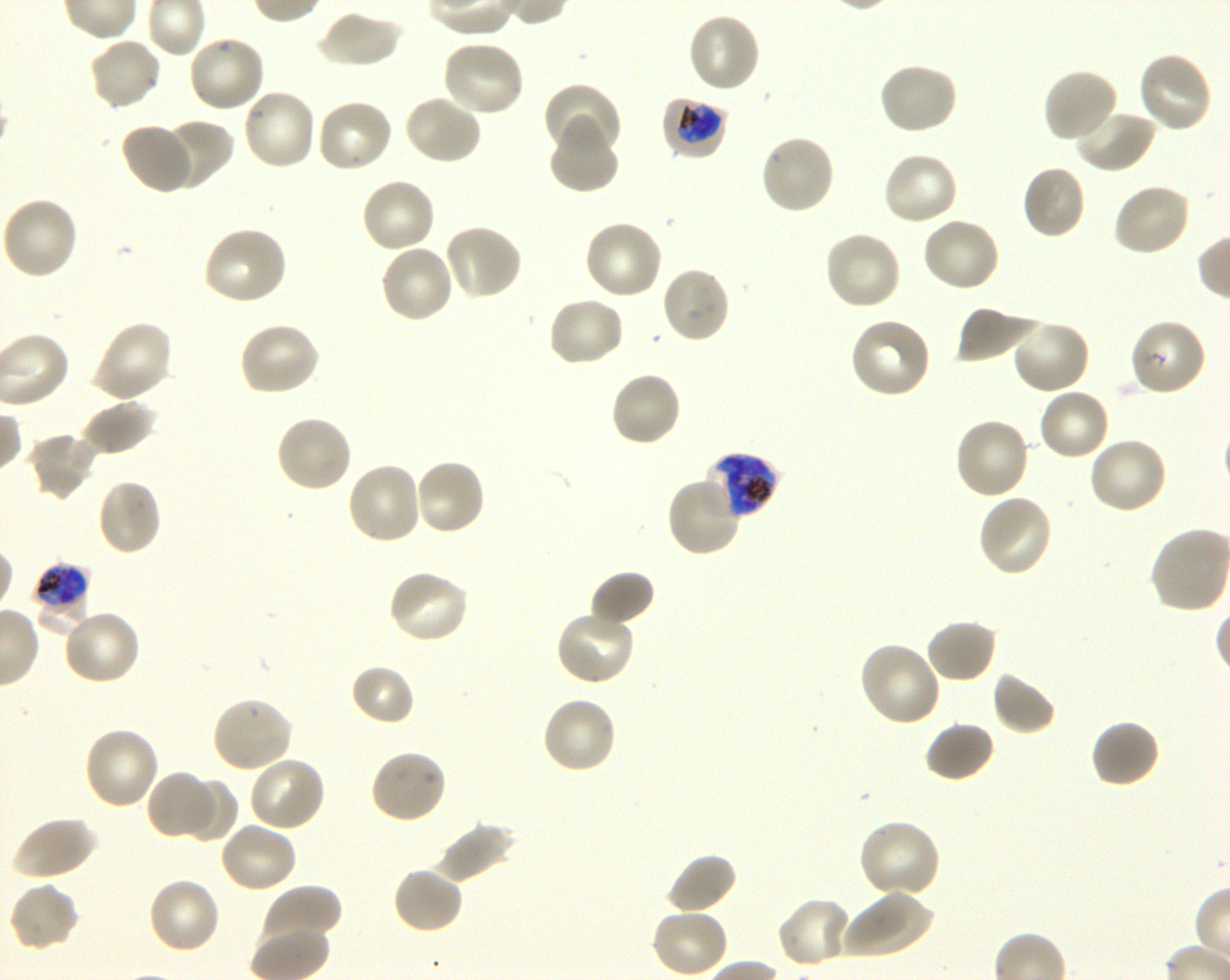

Approximate bounding rectangles given as corner coordinates in pixels from the top-left. Not every red blood cell is marked. A life-cycle stage — or a range of stages, where the recorded stages span more than one — follows each staged infected red blood cell.
Summary:
  - Locations of infected red blood cells: (x1=661, y1=96, x2=728, y2=160) trophozoite; (x1=702, y1=451, x2=780, y2=520) late trophozoite to late schizont; (x1=33, y1=562, x2=90, y2=616) early trophozoite to late schizont
  - Locations of uninfected red blood cells: (x1=316, y1=9, x2=402, y2=68), (x1=686, y1=12, x2=761, y2=94), (x1=187, y1=34, x2=266, y2=113), (x1=88, y1=36, x2=163, y2=111), (x1=441, y1=40, x2=527, y2=118), (x1=1135, y1=51, x2=1213, y2=135), (x1=876, y1=62, x2=959, y2=137), (x1=1043, y1=69, x2=1120, y2=145), (x1=543, y1=83, x2=622, y2=162), (x1=241, y1=87, x2=318, y2=171), (x1=403, y1=93, x2=482, y2=166), (x1=315, y1=97, x2=394, y2=174), (x1=1073, y1=108, x2=1156, y2=174), (x1=159, y1=119, x2=232, y2=190), (x1=548, y1=122, x2=619, y2=194), (x1=119, y1=123, x2=196, y2=194), (x1=759, y1=133, x2=837, y2=216), (x1=881, y1=151, x2=959, y2=227), (x1=1021, y1=164, x2=1087, y2=240), (x1=359, y1=177, x2=436, y2=254), (x1=1112, y1=182, x2=1192, y2=258), (x1=0, y1=196, x2=80, y2=281), (x1=921, y1=216, x2=1002, y2=294), (x1=583, y1=218, x2=664, y2=300), (x1=442, y1=223, x2=523, y2=301), (x1=202, y1=226, x2=289, y2=307), (x1=822, y1=229, x2=903, y2=311), (x1=379, y1=243, x2=455, y2=324), (x1=659, y1=266, x2=731, y2=344), (x1=545, y1=296, x2=626, y2=368), (x1=955, y1=305, x2=1039, y2=365), (x1=849, y1=316, x2=932, y2=399), (x1=1010, y1=318, x2=1092, y2=395), (x1=91, y1=319, x2=173, y2=403), (x1=237, y1=321, x2=321, y2=396), (x1=607, y1=370, x2=682, y2=448), (x1=1037, y1=388, x2=1111, y2=462), (x1=80, y1=399, x2=157, y2=456), (x1=274, y1=414, x2=353, y2=494), (x1=953, y1=416, x2=1032, y2=501), (x1=26, y1=430, x2=100, y2=501), (x1=1087, y1=436, x2=1169, y2=515), (x1=413, y1=457, x2=486, y2=537), (x1=345, y1=462, x2=424, y2=546), (x1=666, y1=474, x2=744, y2=558), (x1=96, y1=479, x2=163, y2=556), (x1=977, y1=493, x2=1054, y2=578), (x1=387, y1=568, x2=471, y2=646), (x1=589, y1=570, x2=655, y2=628), (x1=62, y1=608, x2=142, y2=687), (x1=554, y1=609, x2=636, y2=687), (x1=925, y1=618, x2=998, y2=684), (x1=857, y1=640, x2=942, y2=728), (x1=350, y1=663, x2=416, y2=726), (x1=991, y1=671, x2=1058, y2=736), (x1=211, y1=695, x2=295, y2=773), (x1=541, y1=696, x2=618, y2=775), (x1=1090, y1=718, x2=1161, y2=789), (x1=924, y1=720, x2=996, y2=782), (x1=82, y1=727, x2=160, y2=811), (x1=368, y1=748, x2=447, y2=825), (x1=248, y1=755, x2=327, y2=832), (x1=147, y1=769, x2=214, y2=841), (x1=181, y1=777, x2=238, y2=843), (x1=11, y1=816, x2=97, y2=881), (x1=856, y1=818, x2=942, y2=899), (x1=218, y1=820, x2=299, y2=894), (x1=434, y1=821, x2=515, y2=883), (x1=665, y1=852, x2=738, y2=917), (x1=392, y1=866, x2=464, y2=934), (x1=146, y1=877, x2=221, y2=955), (x1=7, y1=880, x2=80, y2=953), (x1=260, y1=885, x2=341, y2=950), (x1=842, y1=888, x2=935, y2=959), (x1=776, y1=896, x2=854, y2=970), (x1=650, y1=907, x2=729, y2=978)
  - Locations of red blood cells of indeterminate infection status: (x1=1128, y1=317, x2=1208, y2=396)
  - Field of view: one from this slide
  - Objective: 100x, oil immersion, numerical aperture 1.30
  - Preparation: thin blood film
  - Stain: Giemsa
  - Donor blood group: O+
  - Image size: 1230×980 pixels
  - Culture: P. falciparum strain 3D7, shaking, in vitro